State the blood parasite species.
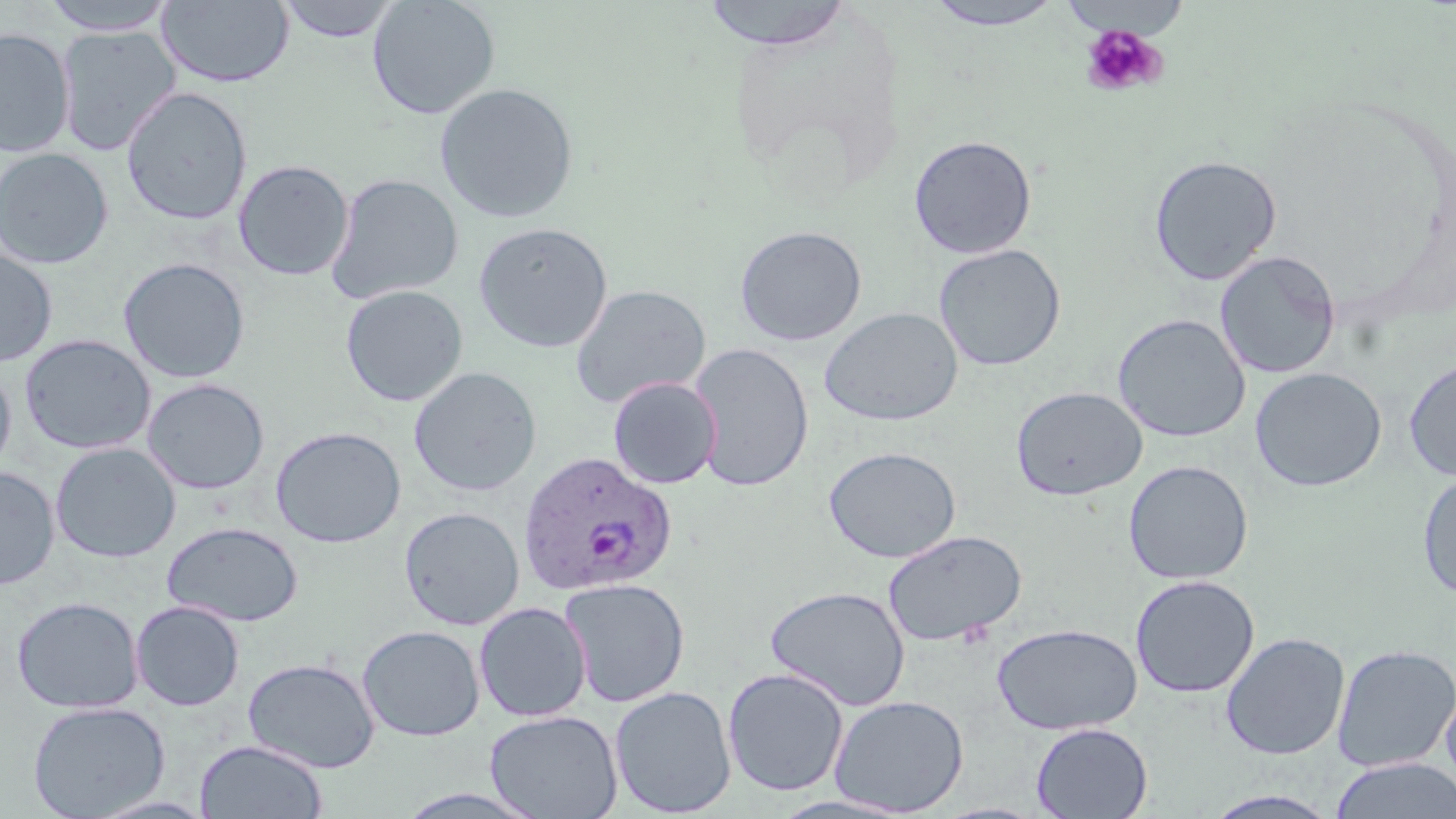

Plasmodium ovale.

Approximate bounding boxes as [x1, y1, x2, y2] in pixels. Platelet locations: [1079, 23, 1168, 98]. Uninfected red blood cell locations: [38, 0, 180, 35], [157, 0, 294, 88], [277, 0, 401, 44], [366, 0, 501, 119], [700, 1, 855, 49], [923, 1, 1067, 30], [56, 26, 181, 156], [0, 28, 74, 158], [435, 82, 578, 223], [121, 87, 252, 225], [908, 134, 1038, 259], [0, 148, 113, 269], [1148, 154, 1282, 285], [233, 160, 354, 281], [326, 173, 464, 305], [473, 222, 613, 353], [733, 224, 868, 346], [933, 243, 1066, 371], [0, 247, 58, 367], [1214, 250, 1341, 379], [118, 257, 250, 384], [340, 285, 468, 407], [570, 285, 711, 409], [819, 307, 963, 427], [1112, 314, 1251, 443], [19, 333, 156, 455], [688, 342, 814, 492], [1403, 357, 1456, 482], [0, 364, 16, 480], [408, 367, 542, 497], [1250, 367, 1387, 492], [608, 377, 722, 489], [142, 378, 270, 495], [1011, 386, 1147, 501], [270, 426, 406, 548], [50, 442, 181, 563], [824, 445, 961, 563], [1123, 460, 1254, 585], [0, 466, 59, 590], [1416, 472, 1456, 600], [399, 507, 525, 630], [161, 521, 304, 626], [883, 529, 1026, 648], [1130, 574, 1260, 698], [560, 577, 690, 707], [765, 585, 911, 710], [12, 596, 143, 713], [131, 600, 245, 711], [473, 601, 592, 722], [991, 622, 1143, 735], [357, 625, 485, 742], [1220, 632, 1350, 760], [1332, 644, 1456, 771], [242, 657, 381, 773], [722, 668, 850, 796], [1439, 678, 1456, 794], [610, 686, 737, 817], [829, 694, 969, 816], [27, 700, 169, 818], [484, 710, 623, 819], [1030, 722, 1153, 819], [195, 740, 327, 819], [1329, 757, 1456, 819], [1201, 790, 1342, 819]. Plasmodium ovale-infected red blood cell locations: [517, 451, 677, 597]. Single field of view. Image is 1456×819 pixels. Thin blood smear. 1000x magnification. May-Grünwald-Giemsa-stained preparation. Optical microscopy.